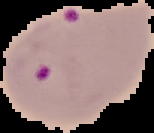
Summary:
  - Malaria status: parasitized
  - Preparation: thin blood film
  - Image size: 154×133 pixels
  - Image type: cell region segmented out of the field of view; surrounding area masked to black